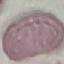

{
  "malaria_status": "uninfected",
  "preparation": "thin smear",
  "stain": "Giemsa",
  "image_type": "cell patch, automatically extracted from a larger field of view and resized to 64 × 64 pixels",
  "capture": "smartphone camera at the microscope eyepiece"
}